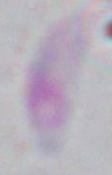
modality = micrograph
magnification = 1000x
identification = Toxoplasma gondii